Assess this cell for malaria.
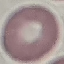

It is uninfected.

Acquired by smartphone through the microscope eyepiece. Thin blood smear. Cell patch, automatically extracted from a larger field of view and resized to 64 × 64 pixels. Giemsa stain.